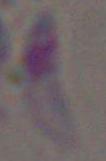

Summary:
  - Modality: micrograph
  - Magnification: 1000x
  - Identification: Toxoplasma gondii